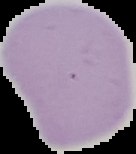

image size = 136×154 pixels
preparation = thin blood smear
image type = segmented cell region with the area outside set to black
result = negative for malaria parasites